Give a bounding box for every Plasmodium parasite.
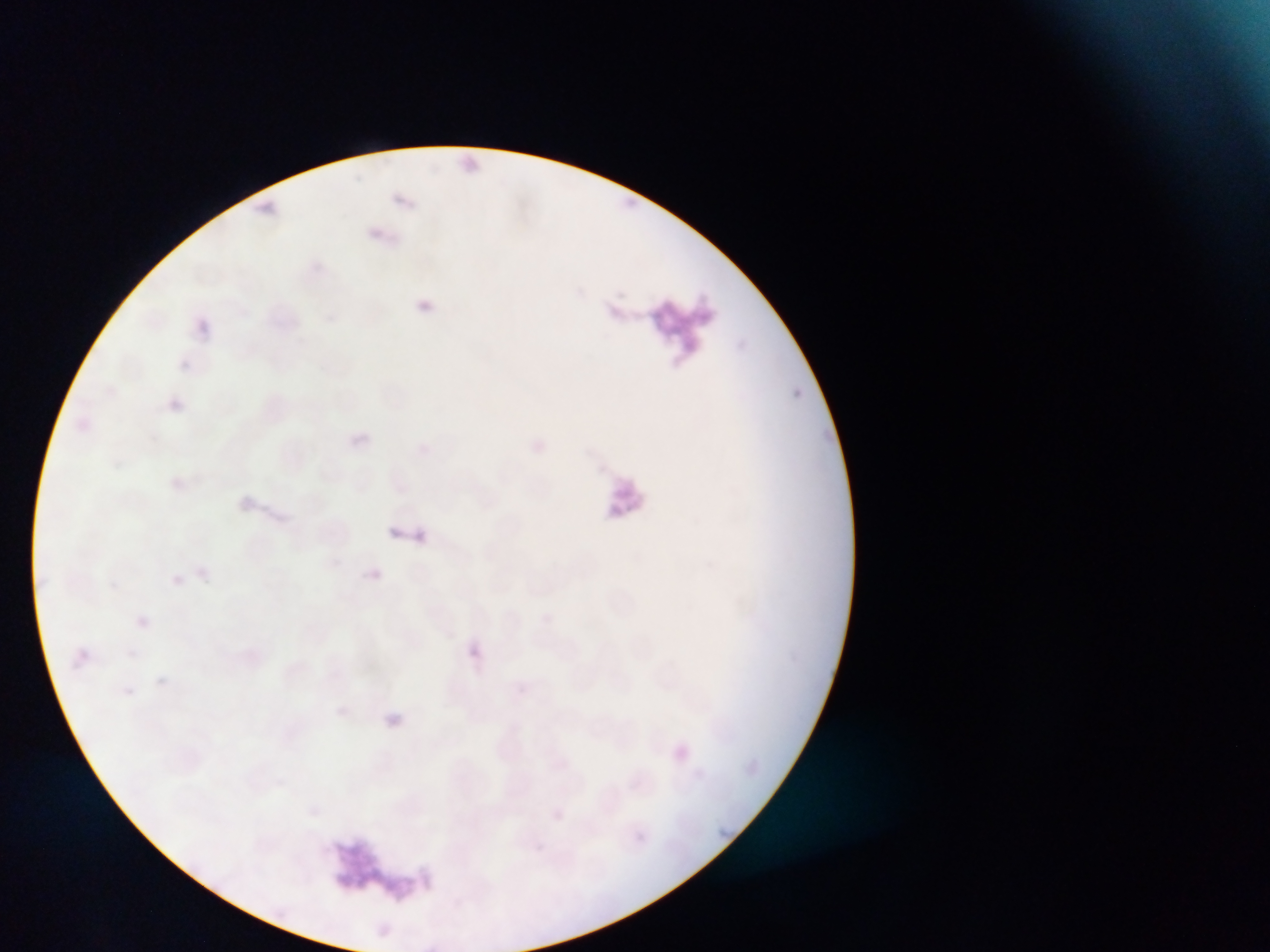

Approximate bounding boxes as [left, top, right, bottom] in pixels.
Plasmodium parasites: [464, 153, 480, 168], [389, 526, 400, 536], [370, 568, 383, 580], [171, 574, 184, 585], [541, 613, 552, 624], [136, 615, 149, 628], [468, 647, 480, 660], [156, 677, 167, 687], [516, 682, 526, 693], [125, 686, 134, 695], [509, 721, 522, 733], [675, 746, 689, 759], [308, 806, 320, 816], [553, 808, 566, 822], [637, 832, 646, 839].

country: Ghana
preparation: thin blood film
image_size: 1270×952 pixels
artifact_stain_precipitate_or_debris_locations: 'approximate bounding boxes as [left, top, right, bottom] in pixels: [632, 290, 716, 379], [580, 464, 663, 524], [332, 837, 416, 910]'
field_of_view: single
capture: mobile-phone photograph through a microscope